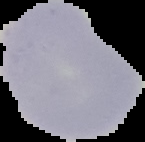

image size = 145×142 pixels
image type = segmented cell region with the area outside set to black
preparation = thin blood film
result = negative for Plasmodium parasites